Locate and identify every blood parasite.
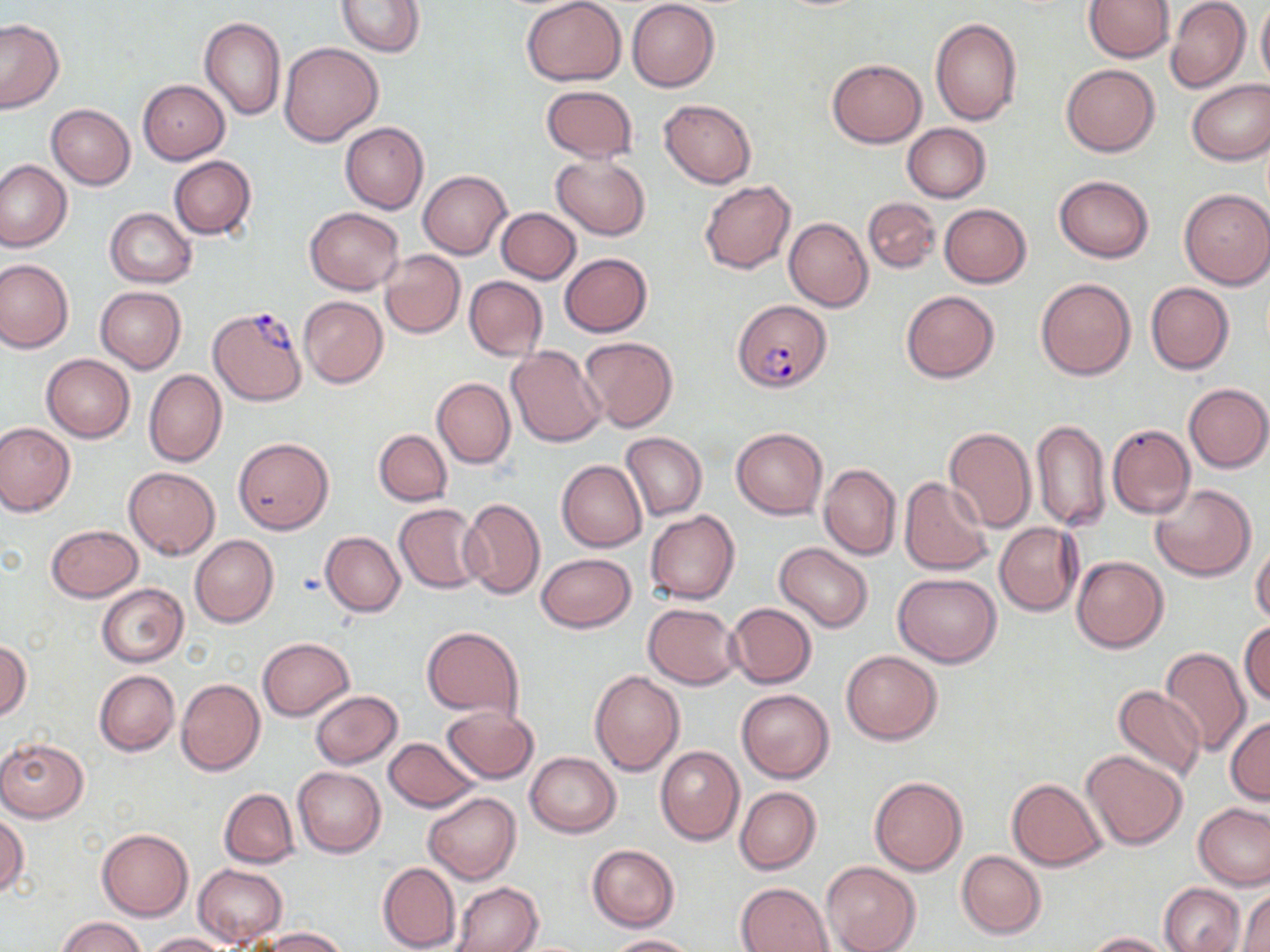
Approximate bounding boxes as [x1, y1, x2, y2] in pixels.
Plasmodium falciparum-infected red blood cells: [734, 300, 832, 391], [208, 306, 307, 406].
No Plasmodium ovale, Plasmodium malariae, Plasmodium vivax, Babesia divergens, or Trypanosoma brucei observed.

Summary:
  - Uninfected red blood cell locations: [521, 0, 626, 86], [627, 0, 718, 91], [1084, 0, 1175, 62], [336, 1, 424, 57], [1256, 1, 1270, 90], [1165, 2, 1251, 92], [200, 16, 286, 120], [930, 17, 1023, 127], [0, 19, 65, 113], [279, 43, 382, 145], [827, 59, 927, 148], [1062, 63, 1159, 156], [1186, 79, 1270, 165], [137, 80, 231, 163], [541, 85, 638, 162], [658, 98, 757, 189], [46, 104, 136, 190], [340, 122, 428, 214], [902, 123, 992, 203], [168, 155, 256, 239], [551, 155, 651, 239], [0, 159, 71, 252], [418, 171, 511, 259], [1054, 175, 1153, 262], [699, 181, 796, 273], [1179, 188, 1270, 289], [863, 197, 940, 274], [940, 204, 1031, 287], [305, 207, 405, 294], [105, 208, 197, 288], [496, 208, 581, 284], [784, 218, 872, 311], [380, 250, 465, 338], [560, 254, 652, 337], [0, 259, 74, 353], [464, 276, 547, 362], [1036, 278, 1136, 380], [1145, 282, 1234, 375], [96, 286, 187, 373], [901, 290, 1000, 383], [298, 296, 388, 388], [579, 337, 679, 432], [506, 345, 606, 447], [42, 353, 135, 442], [144, 369, 227, 467], [432, 378, 515, 469], [1184, 383, 1269, 473], [1111, 408, 1260, 510], [1032, 419, 1110, 530], [0, 422, 75, 516], [1107, 424, 1195, 519], [943, 427, 1037, 534], [732, 428, 827, 518], [373, 429, 451, 506], [622, 432, 707, 521], [233, 436, 334, 533], [557, 460, 646, 551], [819, 462, 900, 560], [123, 465, 220, 559], [899, 477, 995, 577], [1151, 483, 1255, 582], [459, 497, 546, 600], [393, 504, 487, 594], [646, 511, 740, 604], [994, 522, 1082, 616], [44, 525, 143, 602], [321, 531, 405, 616], [190, 535, 278, 627], [1251, 541, 1270, 627], [775, 543, 873, 632], [535, 553, 636, 632], [1072, 556, 1168, 652], [893, 573, 1001, 667], [96, 583, 189, 667], [644, 603, 741, 690], [725, 603, 816, 688], [1240, 621, 1270, 708], [421, 625, 525, 719], [258, 638, 354, 721], [0, 639, 31, 720], [1160, 646, 1250, 756], [841, 650, 942, 743], [94, 669, 179, 756], [590, 670, 686, 776], [176, 679, 265, 776], [1112, 683, 1207, 782], [736, 687, 834, 783], [310, 690, 402, 768], [442, 705, 538, 784], [1225, 716, 1270, 804], [0, 737, 90, 821], [384, 737, 479, 812], [655, 746, 744, 845], [1081, 749, 1189, 850], [525, 751, 620, 837], [293, 767, 385, 857], [868, 777, 967, 874], [1006, 778, 1107, 869], [734, 786, 822, 875], [219, 788, 299, 867], [423, 791, 521, 883], [1193, 803, 1270, 889], [0, 813, 28, 897], [97, 828, 192, 920], [587, 843, 679, 931], [957, 851, 1046, 938], [822, 861, 920, 951], [377, 862, 460, 952], [193, 864, 287, 946], [453, 882, 543, 952], [737, 882, 833, 952], [1159, 882, 1245, 952], [1239, 888, 1270, 951], [56, 915, 148, 952], [260, 928, 346, 951], [1086, 931, 1177, 951], [145, 932, 230, 951], [606, 934, 695, 951]
  - Slide-level diagnosis: Plasmodium falciparum
  - Image size: 1270×952 pixels
  - Preparation: thin blood film
  - Field of view: one of a larger specimen
  - Modality: optical microscopy
  - Magnification: 1000x
  - Stain: May-Grünwald-Giemsa